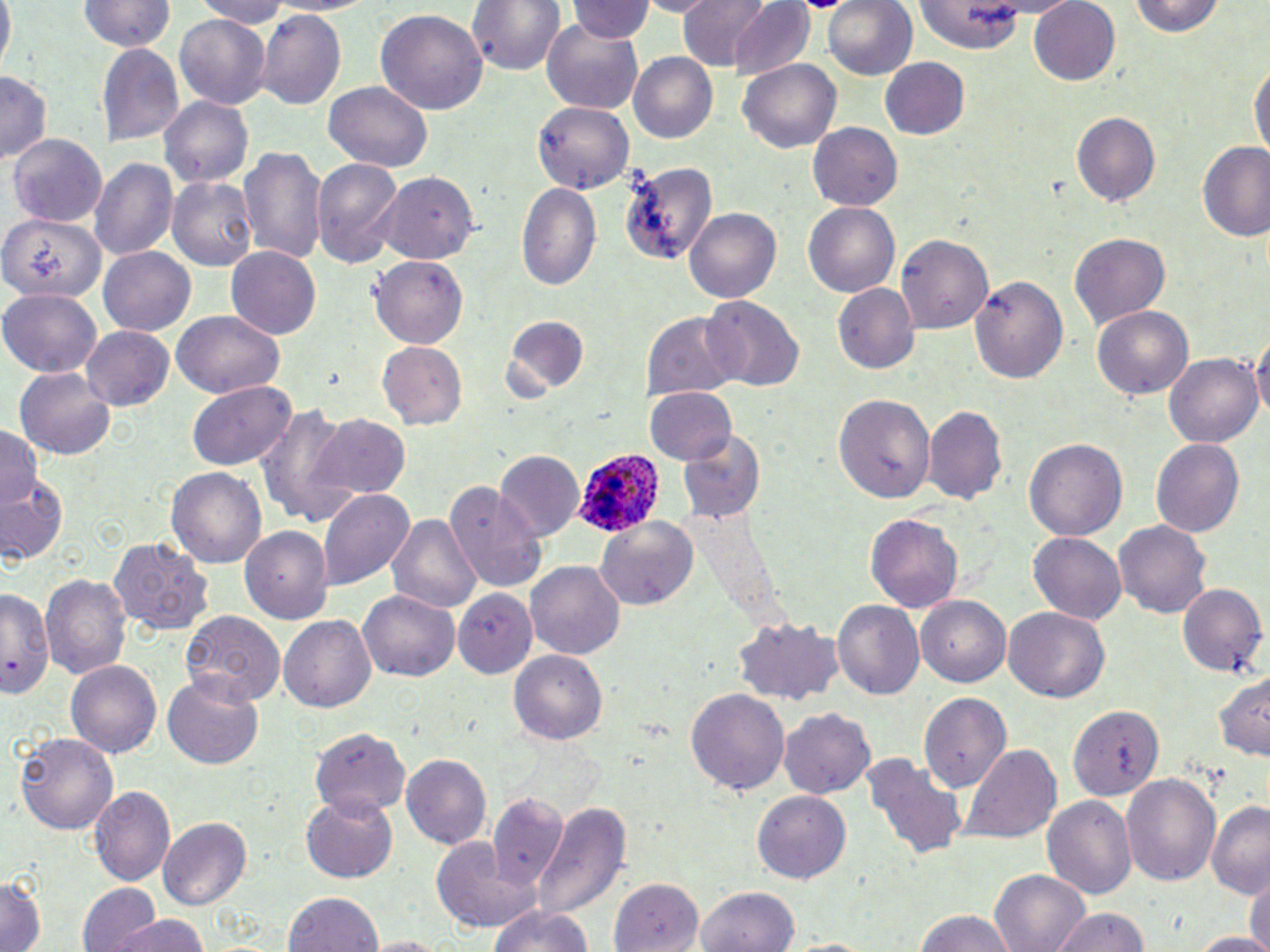

slide-level diagnosis = Plasmodium ovale
image size = 1270×952 pixels
modality = optical microscopy
preparation = thin blood smear
uninfected red blood cell locations = approximate bounding boxes as named x1/y1/x2/y2 corners in pixels: (x1=0, y1=0, x2=15, y2=65), (x1=195, y1=0, x2=297, y2=27), (x1=258, y1=0, x2=371, y2=17), (x1=470, y1=0, x2=564, y2=77), (x1=676, y1=0, x2=773, y2=70), (x1=821, y1=0, x2=916, y2=81), (x1=1127, y1=0, x2=1226, y2=38), (x1=77, y1=1, x2=174, y2=52), (x1=726, y1=1, x2=817, y2=81), (x1=1027, y1=1, x2=1121, y2=86), (x1=569, y1=2, x2=654, y2=44), (x1=914, y1=3, x2=1032, y2=52), (x1=258, y1=9, x2=345, y2=110), (x1=376, y1=10, x2=488, y2=115), (x1=175, y1=14, x2=271, y2=109), (x1=541, y1=20, x2=644, y2=112), (x1=97, y1=42, x2=184, y2=145), (x1=628, y1=52, x2=719, y2=143), (x1=881, y1=58, x2=971, y2=141), (x1=1251, y1=58, x2=1269, y2=162), (x1=739, y1=60, x2=842, y2=153), (x1=0, y1=74, x2=51, y2=162), (x1=324, y1=80, x2=431, y2=171), (x1=160, y1=98, x2=253, y2=186), (x1=534, y1=99, x2=635, y2=192), (x1=1072, y1=109, x2=1162, y2=206), (x1=809, y1=122, x2=905, y2=212), (x1=9, y1=132, x2=108, y2=228), (x1=1197, y1=142, x2=1270, y2=242), (x1=239, y1=144, x2=326, y2=265), (x1=89, y1=155, x2=177, y2=262), (x1=312, y1=156, x2=405, y2=270), (x1=617, y1=156, x2=718, y2=266), (x1=375, y1=172, x2=481, y2=263), (x1=168, y1=175, x2=257, y2=271), (x1=517, y1=182, x2=600, y2=289), (x1=803, y1=201, x2=900, y2=298), (x1=684, y1=207, x2=782, y2=302), (x1=2, y1=215, x2=105, y2=305), (x1=1070, y1=233, x2=1170, y2=325), (x1=894, y1=234, x2=992, y2=333), (x1=226, y1=247, x2=321, y2=340), (x1=100, y1=249, x2=195, y2=335), (x1=370, y1=253, x2=469, y2=346), (x1=968, y1=272, x2=1068, y2=386), (x1=834, y1=283, x2=920, y2=375), (x1=0, y1=289, x2=101, y2=375), (x1=703, y1=296, x2=802, y2=391), (x1=1092, y1=305, x2=1193, y2=399), (x1=170, y1=310, x2=287, y2=398), (x1=643, y1=310, x2=741, y2=400), (x1=502, y1=317, x2=595, y2=398), (x1=1253, y1=325, x2=1270, y2=432), (x1=82, y1=326, x2=173, y2=409), (x1=375, y1=341, x2=468, y2=429), (x1=1164, y1=352, x2=1262, y2=447), (x1=12, y1=367, x2=117, y2=460), (x1=187, y1=383, x2=295, y2=470), (x1=644, y1=387, x2=737, y2=467), (x1=834, y1=393, x2=937, y2=505), (x1=255, y1=405, x2=361, y2=527), (x1=924, y1=406, x2=1007, y2=504), (x1=311, y1=415, x2=411, y2=501), (x1=0, y1=425, x2=46, y2=508), (x1=679, y1=430, x2=767, y2=525), (x1=1023, y1=438, x2=1128, y2=544), (x1=1151, y1=438, x2=1245, y2=540), (x1=495, y1=451, x2=583, y2=540), (x1=168, y1=467, x2=267, y2=570), (x1=0, y1=474, x2=69, y2=565), (x1=443, y1=481, x2=549, y2=594), (x1=317, y1=488, x2=415, y2=589), (x1=866, y1=513, x2=964, y2=612), (x1=387, y1=514, x2=481, y2=615), (x1=594, y1=514, x2=699, y2=610), (x1=1113, y1=521, x2=1212, y2=618), (x1=240, y1=525, x2=335, y2=623), (x1=1028, y1=531, x2=1127, y2=624), (x1=110, y1=538, x2=212, y2=635), (x1=527, y1=561, x2=625, y2=662), (x1=40, y1=572, x2=131, y2=682), (x1=1177, y1=583, x2=1269, y2=678), (x1=0, y1=585, x2=56, y2=701), (x1=357, y1=586, x2=458, y2=679), (x1=455, y1=588, x2=538, y2=675), (x1=917, y1=596, x2=1013, y2=686), (x1=833, y1=600, x2=925, y2=699), (x1=1004, y1=606, x2=1110, y2=702), (x1=181, y1=607, x2=284, y2=708), (x1=279, y1=616, x2=375, y2=713), (x1=733, y1=617, x2=844, y2=704), (x1=511, y1=648, x2=608, y2=742), (x1=68, y1=661, x2=161, y2=761), (x1=1213, y1=670, x2=1269, y2=762), (x1=163, y1=676, x2=262, y2=769), (x1=687, y1=687, x2=789, y2=798), (x1=918, y1=692, x2=1010, y2=794), (x1=1069, y1=705, x2=1165, y2=799), (x1=781, y1=707, x2=875, y2=799), (x1=310, y1=727, x2=410, y2=816), (x1=15, y1=731, x2=119, y2=834), (x1=958, y1=744, x2=1062, y2=845), (x1=402, y1=754, x2=491, y2=851), (x1=865, y1=755, x2=965, y2=859), (x1=1121, y1=772, x2=1223, y2=886), (x1=92, y1=785, x2=176, y2=887), (x1=752, y1=790, x2=851, y2=885), (x1=300, y1=791, x2=399, y2=882), (x1=486, y1=794, x2=572, y2=899), (x1=1042, y1=794, x2=1137, y2=899), (x1=533, y1=800, x2=629, y2=919), (x1=1208, y1=800, x2=1270, y2=896), (x1=159, y1=819, x2=252, y2=910), (x1=429, y1=837, x2=542, y2=935), (x1=991, y1=868, x2=1091, y2=952), (x1=1246, y1=870, x2=1268, y2=952), (x1=0, y1=875, x2=45, y2=952), (x1=611, y1=877, x2=702, y2=952), (x1=78, y1=884, x2=160, y2=952), (x1=694, y1=887, x2=800, y2=952), (x1=284, y1=890, x2=384, y2=951), (x1=487, y1=904, x2=598, y2=952), (x1=1055, y1=907, x2=1151, y2=952), (x1=911, y1=908, x2=1014, y2=952), (x1=112, y1=913, x2=214, y2=952), (x1=1187, y1=932, x2=1270, y2=952), (x1=365, y1=935, x2=453, y2=952), (x1=777, y1=936, x2=886, y2=951)
field of view = single
Plasmodium ovale-infected red blood cell locations = approximate bounding boxes as named x1/y1/x2/y2 corners in pixels: (x1=571, y1=449, x2=663, y2=540)
stain = May-Grünwald-Giemsa
magnification = 1000x